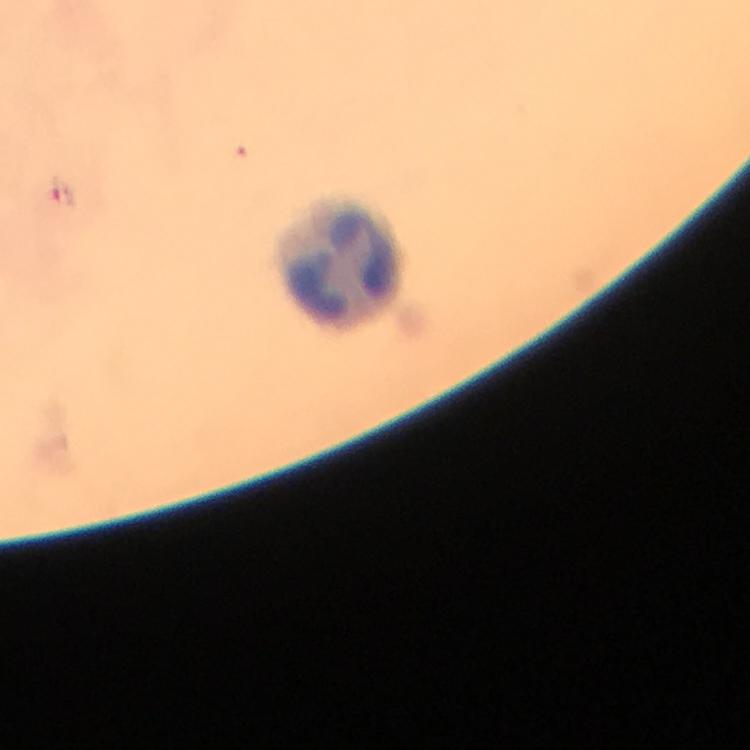

preparation = thick blood smear
image size = 750×750 pixels
capture = smartphone camera through the microscope
immersion oil = used
stain = Giemsa
leukocyte locations = approximate object centers, in pixels from the top-left corner: (x=345, y=262)
context = from a malaria diagnostic workup
cropped from = one field of view
magnification = 100x
Plasmodium parasite locations = approximate object centers, in pixels from the top-left corner: (x=65, y=195)